State which parasite is depicted.
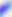

This is Toxoplasma gondii.

Photomicrograph. 400x magnification.